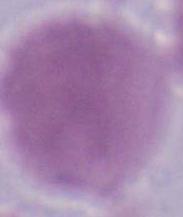
Summary:
  - Modality: photomicrograph
  - Identification: erythrocyte
  - Magnification: 1000x